Assess this cell for malaria.
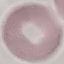

It is uninfected.

Photographed with a smartphone camera at the microscope eyepiece. Giemsa-stained preparation. Thin blood film. Cell patch, automatically extracted from a larger field of view and resized to 64 × 64 pixels.